Give the preparation type.
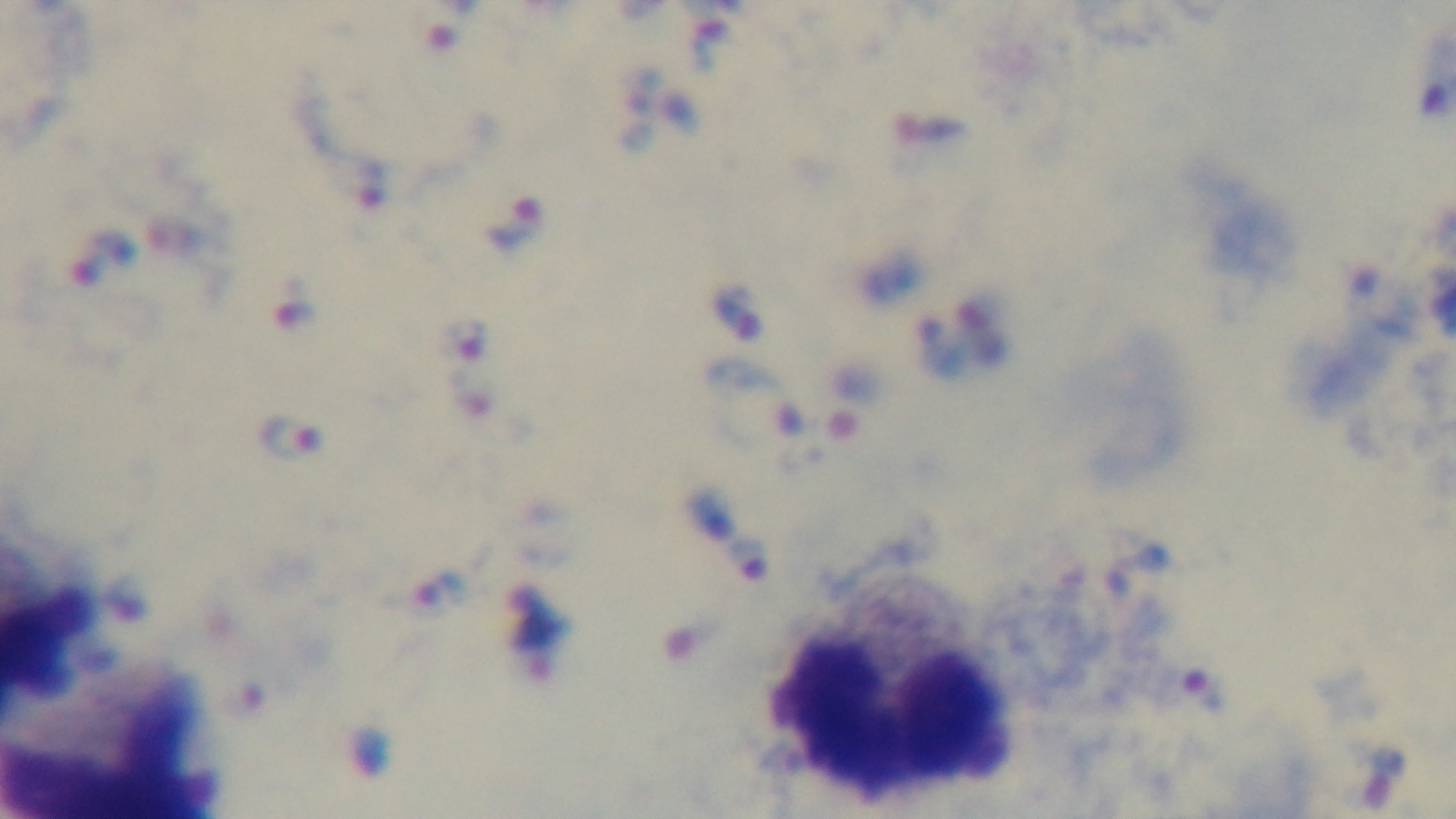

Thick.

{
  "field_of_view": "one from the slide",
  "malaria_status": "infected",
  "capture": "mounted 4K digital camera",
  "modality": "light microscopy",
  "stain": "Giemsa",
  "objective": "100x oil immersion"
}